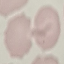 Result: no malaria parasites detected. Giemsa stain. Photographed with a smartphone camera at the microscope eyepiece. Automatically extracted cell patch, resized to 64 × 64 pixels. Thin blood film.